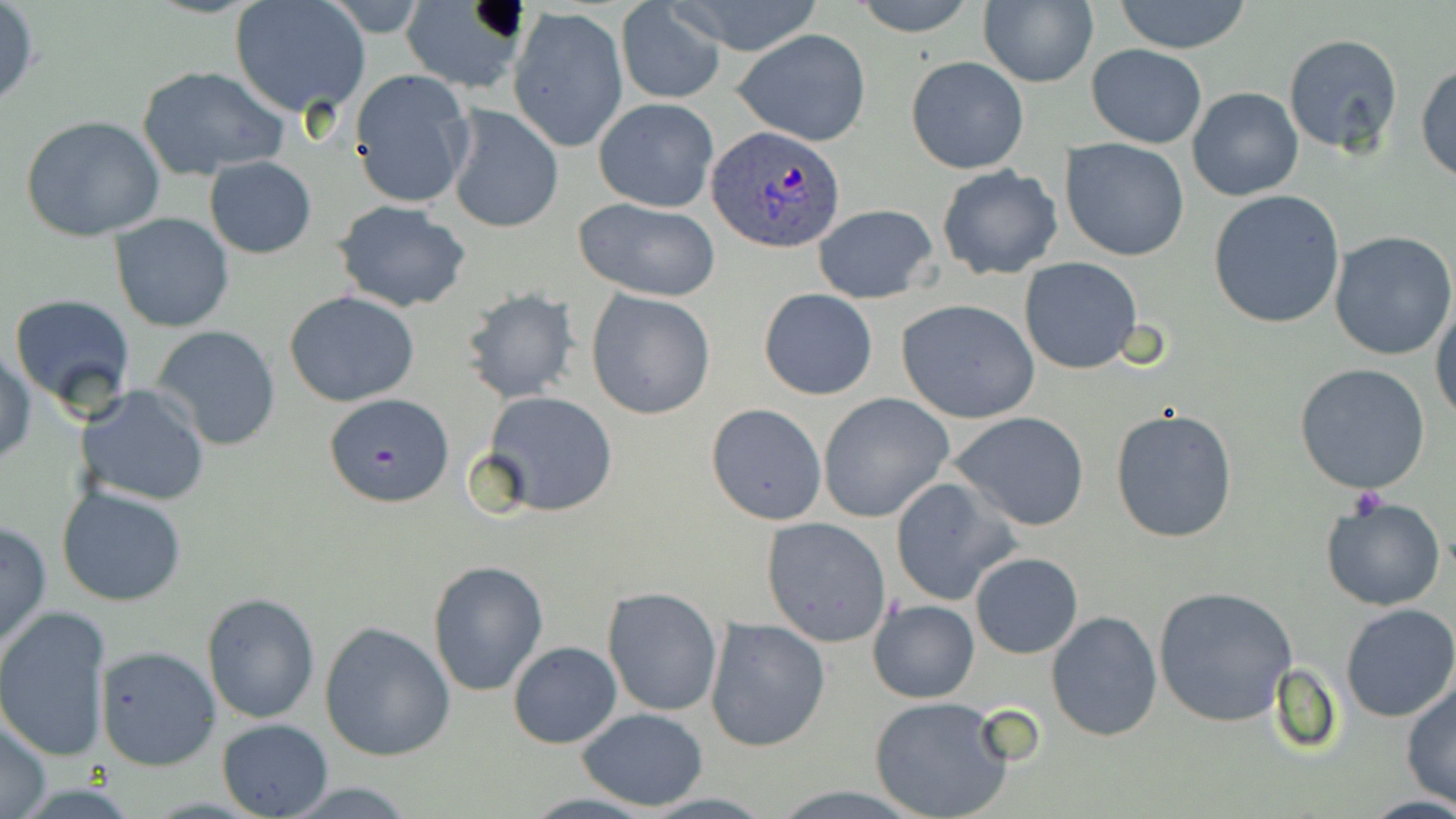
Summary:
  - Coordinate format: approximate bounding boxes as [x1, y1, x2, y2] in pixels
  - Plasmodium ovale-infected red blood cell locations: [708, 127, 846, 252]
  - Uninfected red blood cell locations: [668, 0, 828, 56], [852, 0, 981, 36], [1114, 0, 1254, 54], [229, 1, 370, 118], [615, 2, 726, 104], [977, 2, 1098, 87], [0, 3, 40, 110], [400, 3, 529, 95], [510, 7, 628, 154], [732, 29, 873, 146], [1282, 32, 1404, 158], [1087, 44, 1206, 148], [905, 56, 1030, 175], [1416, 61, 1456, 186], [135, 64, 291, 181], [348, 70, 476, 209], [1188, 86, 1303, 201], [593, 98, 719, 211], [445, 104, 564, 235], [22, 116, 166, 242], [1060, 139, 1190, 261], [203, 157, 317, 258], [936, 165, 1063, 280], [1207, 191, 1349, 329], [572, 198, 722, 302], [332, 199, 472, 312], [814, 204, 939, 304], [111, 213, 234, 332], [1329, 231, 1456, 360], [1019, 258, 1144, 374], [460, 287, 581, 404], [758, 288, 879, 400], [586, 289, 716, 419], [284, 291, 421, 407], [8, 293, 137, 413], [896, 299, 1042, 424], [1431, 300, 1456, 424], [149, 325, 283, 451], [1, 346, 35, 466], [1294, 363, 1432, 493], [76, 383, 208, 508], [478, 390, 619, 518], [324, 392, 454, 506], [817, 393, 954, 522], [705, 403, 827, 526], [1110, 408, 1238, 542], [949, 411, 1091, 532], [890, 476, 1018, 607], [56, 485, 188, 607], [1321, 495, 1444, 612], [762, 517, 891, 647], [0, 520, 52, 654], [970, 553, 1083, 658], [427, 560, 548, 697], [1153, 585, 1298, 728], [602, 587, 721, 716], [203, 592, 320, 723], [868, 599, 979, 704], [1340, 604, 1456, 722], [0, 606, 112, 761], [1046, 610, 1163, 742], [705, 616, 831, 752], [319, 621, 456, 761], [508, 641, 622, 749], [94, 644, 223, 770], [1401, 683, 1456, 807], [869, 696, 1015, 819], [574, 707, 708, 810], [0, 713, 51, 819], [217, 718, 335, 818], [275, 780, 425, 816]
  - Platelet locations: [1348, 487, 1389, 517]
  - Slide-level diagnosis: Plasmodium ovale
  - Stain: May-Grünwald-Giemsa
  - Magnification: 1000x
  - Preparation: thin blood smear
  - Field of view: one of a larger specimen
  - Image size: 1456×819 pixels
  - Modality: light microscopy